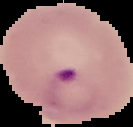

image_type: segmented cell region with the area outside set to black
preparation: thin blood film
malaria_status: parasitized
image_size: 133×127 pixels